Describe the morphology of the erythrocytes.
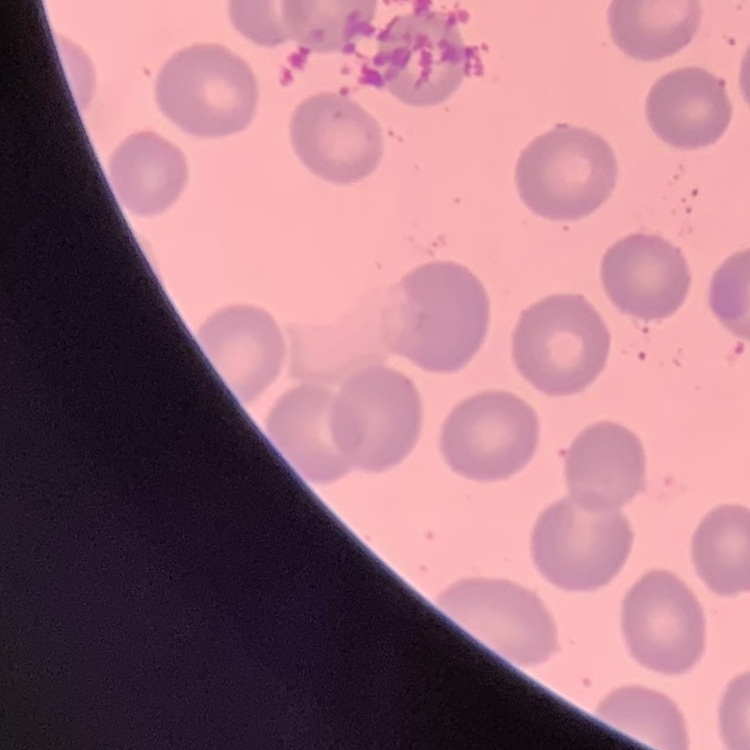
They show no rouleaux formation.

Thin blood smear. Field's or Giemsa stain. One tile cut from a larger photomicrograph.